State which parasite is depicted.
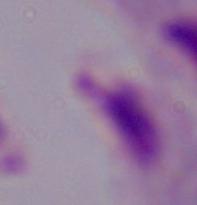

A trichomonad.

magnification = 1000x
modality = photomicrograph